Comment on the morphology of the red blood cells.
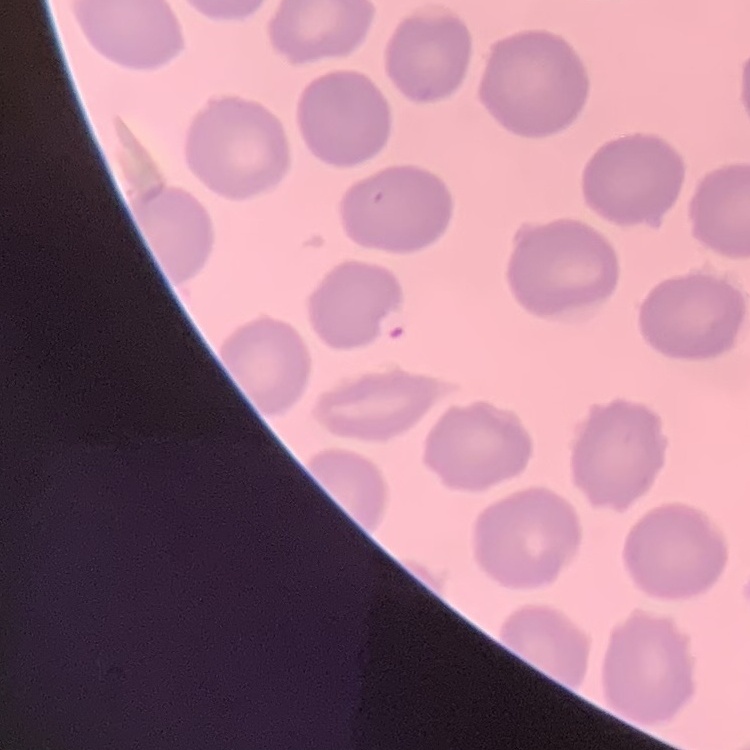

They show no rouleaux formation.

One tile cut from a larger photomicrograph. Thin blood film. Stained with either Field's or Giemsa.